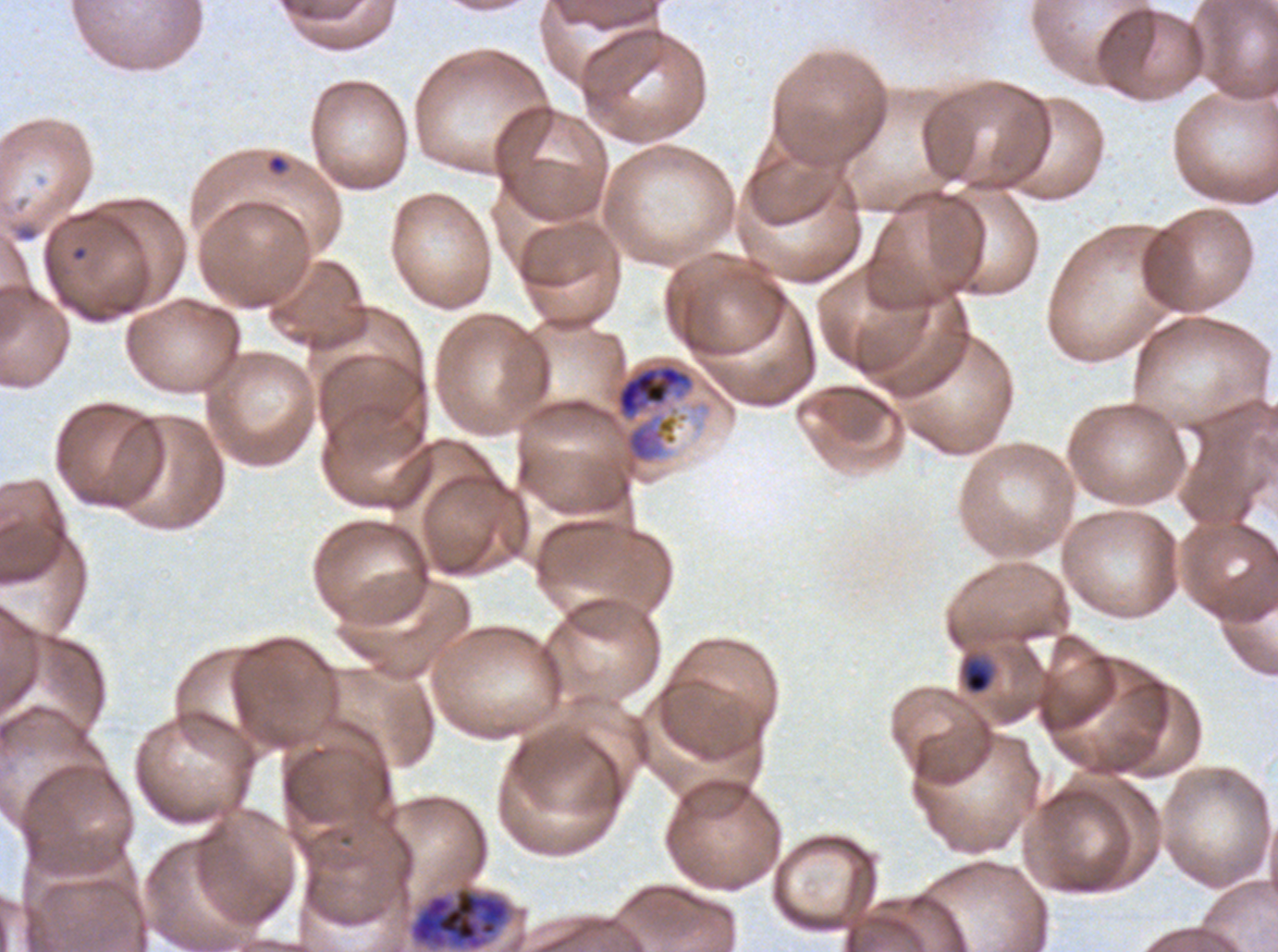

specimen: P. falciparum cultured ex vivo for 24 to 48 hours, from a patient in The Gambia
late_trophozoite_locations: 'approximate bounding rectangles given as corner coordinates in pixels from the top-left: (x1=617, y1=364, x2=691, y2=417)'
late_ring_early_trophozoite_locations: 'approximate bounding rectangles given as corner coordinates in pixels from the top-left: (x1=961, y1=657, x2=994, y2=695)'
preparation: thin blood film
life_cycle_stages_observed: ring, late-ring/early-trophozoite, late trophozoite, late schizont
stain: Giemsa
ring_locations: 'approximate bounding rectangles given as corner coordinates in pixels from the top-left: (x1=266, y1=153, x2=288, y2=175)'
image_size: 1278×952 pixels
late_schizont_locations: 'approximate bounding rectangles given as corner coordinates in pixels from the top-left: (x1=409, y1=886, x2=510, y2=951)'
field_of_view: sub-image separated from a larger composite